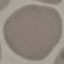

Summary:
  - Result: no malaria parasites seen
  - Capture: smartphone camera at the microscope eyepiece
  - Stain: Giemsa
  - Preparation: thin blood film
  - Image type: cell patch, automatically extracted from a larger field of view and resized to 64 × 64 pixels